Classify this cell by malaria status.
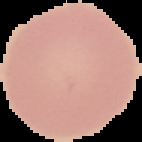
Uninfected.

Summary:
  - Image size: 142×142 pixels
  - Preparation: thin blood smear
  - Image type: segmented cell region on a black background